Give the extent of all uninfected red blood cells.
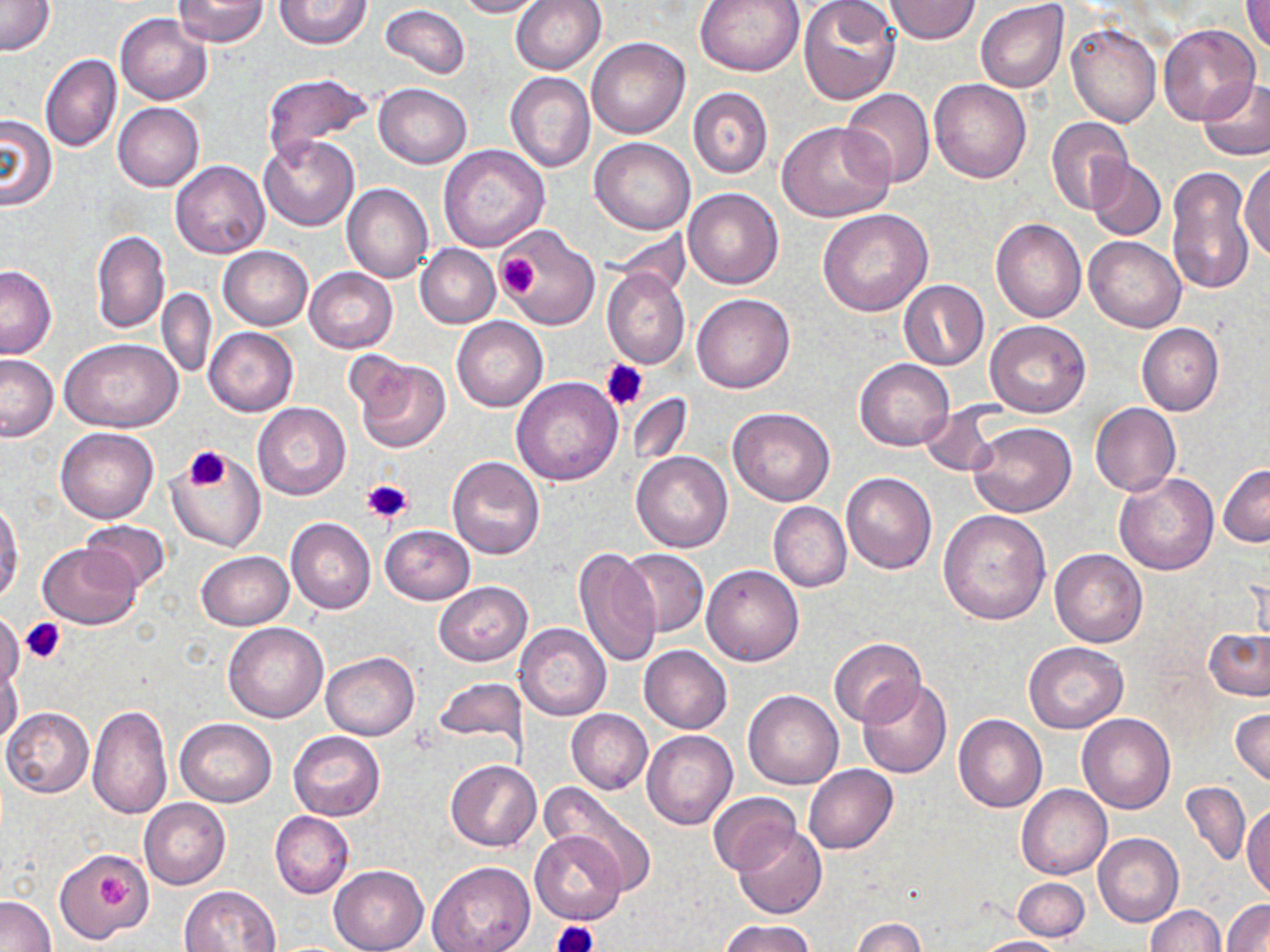

Approximate bounding boxes as named x1/y1/x2/y2 corners in pixels.
Uninfected red blood cells: (x1=171, y1=0, x2=269, y2=47), (x1=275, y1=0, x2=372, y2=49), (x1=454, y1=0, x2=546, y2=17), (x1=511, y1=0, x2=607, y2=74), (x1=695, y1=0, x2=806, y2=76), (x1=798, y1=0, x2=902, y2=105), (x1=882, y1=0, x2=981, y2=45), (x1=1242, y1=0, x2=1270, y2=53), (x1=0, y1=1, x2=56, y2=57), (x1=975, y1=2, x2=1068, y2=93), (x1=379, y1=5, x2=470, y2=81), (x1=116, y1=13, x2=213, y2=105), (x1=1066, y1=21, x2=1161, y2=127), (x1=1157, y1=25, x2=1261, y2=126), (x1=586, y1=38, x2=690, y2=139), (x1=41, y1=53, x2=122, y2=153), (x1=505, y1=71, x2=595, y2=172), (x1=262, y1=73, x2=373, y2=160), (x1=1197, y1=76, x2=1270, y2=161), (x1=929, y1=78, x2=1031, y2=183), (x1=373, y1=83, x2=472, y2=168), (x1=688, y1=86, x2=773, y2=179), (x1=839, y1=88, x2=935, y2=188), (x1=114, y1=103, x2=204, y2=191), (x1=0, y1=115, x2=58, y2=210), (x1=1046, y1=118, x2=1133, y2=215), (x1=778, y1=120, x2=895, y2=222), (x1=259, y1=136, x2=360, y2=230), (x1=589, y1=137, x2=696, y2=234), (x1=439, y1=145, x2=550, y2=252), (x1=1241, y1=157, x2=1270, y2=262), (x1=1086, y1=158, x2=1167, y2=242), (x1=170, y1=161, x2=269, y2=259), (x1=1166, y1=164, x2=1257, y2=295), (x1=342, y1=183, x2=433, y2=283), (x1=684, y1=187, x2=784, y2=289), (x1=819, y1=208, x2=934, y2=316), (x1=991, y1=217, x2=1086, y2=323), (x1=500, y1=225, x2=600, y2=330), (x1=91, y1=230, x2=169, y2=333), (x1=1084, y1=235, x2=1186, y2=332), (x1=415, y1=244, x2=501, y2=327), (x1=218, y1=246, x2=313, y2=330), (x1=0, y1=265, x2=57, y2=357), (x1=305, y1=268, x2=398, y2=352), (x1=601, y1=268, x2=691, y2=371), (x1=899, y1=280, x2=988, y2=370), (x1=158, y1=288, x2=217, y2=379), (x1=693, y1=293, x2=794, y2=393), (x1=451, y1=316, x2=548, y2=411), (x1=987, y1=321, x2=1091, y2=417), (x1=1136, y1=323, x2=1224, y2=415), (x1=205, y1=328, x2=297, y2=416), (x1=61, y1=337, x2=183, y2=432), (x1=0, y1=355, x2=58, y2=441), (x1=354, y1=357, x2=451, y2=455), (x1=854, y1=358, x2=954, y2=451), (x1=512, y1=377, x2=623, y2=485), (x1=627, y1=393, x2=693, y2=466), (x1=1090, y1=402, x2=1181, y2=497), (x1=253, y1=403, x2=351, y2=500), (x1=728, y1=407, x2=835, y2=506), (x1=920, y1=407, x2=998, y2=476), (x1=1101, y1=412, x2=1199, y2=560), (x1=967, y1=422, x2=1077, y2=518), (x1=56, y1=428, x2=159, y2=523), (x1=168, y1=452, x2=267, y2=553), (x1=631, y1=452, x2=732, y2=553), (x1=447, y1=456, x2=545, y2=559), (x1=1218, y1=464, x2=1270, y2=546), (x1=841, y1=472, x2=937, y2=574), (x1=1114, y1=472, x2=1220, y2=575), (x1=0, y1=500, x2=23, y2=606), (x1=768, y1=501, x2=852, y2=592), (x1=938, y1=510, x2=1051, y2=624), (x1=285, y1=517, x2=376, y2=613), (x1=81, y1=519, x2=172, y2=592), (x1=379, y1=525, x2=475, y2=605), (x1=37, y1=542, x2=143, y2=628), (x1=573, y1=546, x2=662, y2=667), (x1=617, y1=548, x2=709, y2=638), (x1=1050, y1=549, x2=1148, y2=647), (x1=197, y1=551, x2=293, y2=629), (x1=702, y1=564, x2=805, y2=666), (x1=434, y1=582, x2=532, y2=666), (x1=0, y1=614, x2=25, y2=689), (x1=223, y1=622, x2=328, y2=723), (x1=514, y1=622, x2=612, y2=721), (x1=1205, y1=628, x2=1270, y2=701), (x1=830, y1=637, x2=927, y2=727), (x1=1023, y1=641, x2=1128, y2=733), (x1=639, y1=645, x2=732, y2=733), (x1=321, y1=652, x2=419, y2=739), (x1=0, y1=661, x2=23, y2=746), (x1=433, y1=678, x2=527, y2=748), (x1=857, y1=678, x2=952, y2=779), (x1=743, y1=690, x2=843, y2=790), (x1=88, y1=702, x2=173, y2=819), (x1=2, y1=707, x2=94, y2=797), (x1=1232, y1=708, x2=1270, y2=785), (x1=566, y1=709, x2=653, y2=794), (x1=1077, y1=713, x2=1175, y2=814), (x1=954, y1=714, x2=1047, y2=812), (x1=175, y1=719, x2=277, y2=807), (x1=642, y1=730, x2=738, y2=830), (x1=289, y1=731, x2=384, y2=820), (x1=446, y1=759, x2=542, y2=851), (x1=804, y1=764, x2=898, y2=853), (x1=537, y1=782, x2=658, y2=894), (x1=1181, y1=782, x2=1251, y2=866), (x1=1017, y1=784, x2=1112, y2=880), (x1=708, y1=792, x2=802, y2=874), (x1=140, y1=799, x2=231, y2=889), (x1=1243, y1=801, x2=1270, y2=900), (x1=270, y1=811, x2=355, y2=898), (x1=733, y1=823, x2=827, y2=920), (x1=530, y1=830, x2=627, y2=924), (x1=1093, y1=833, x2=1182, y2=927), (x1=55, y1=847, x2=151, y2=941), (x1=427, y1=862, x2=535, y2=952), (x1=328, y1=865, x2=429, y2=952), (x1=1013, y1=878, x2=1089, y2=941), (x1=178, y1=884, x2=283, y2=951), (x1=1, y1=895, x2=55, y2=952), (x1=1222, y1=900, x2=1270, y2=952), (x1=1145, y1=905, x2=1224, y2=952), (x1=852, y1=917, x2=925, y2=952), (x1=719, y1=919, x2=815, y2=952), (x1=971, y1=936, x2=1069, y2=952).

Platelet locations: (x1=495, y1=251, x2=540, y2=297), (x1=600, y1=359, x2=648, y2=410), (x1=184, y1=447, x2=229, y2=491), (x1=361, y1=478, x2=413, y2=526), (x1=21, y1=619, x2=66, y2=664), (x1=99, y1=873, x2=131, y2=908), (x1=552, y1=921, x2=595, y2=952). Slide-level diagnosis: negative for blood parasites. May-Grünwald-Giemsa-stained preparation. Thin blood film. 1000x magnification. Image is 1270×952 pixels. Optical microscopy. Single field of view.